Describe the morphology of the red blood cells.
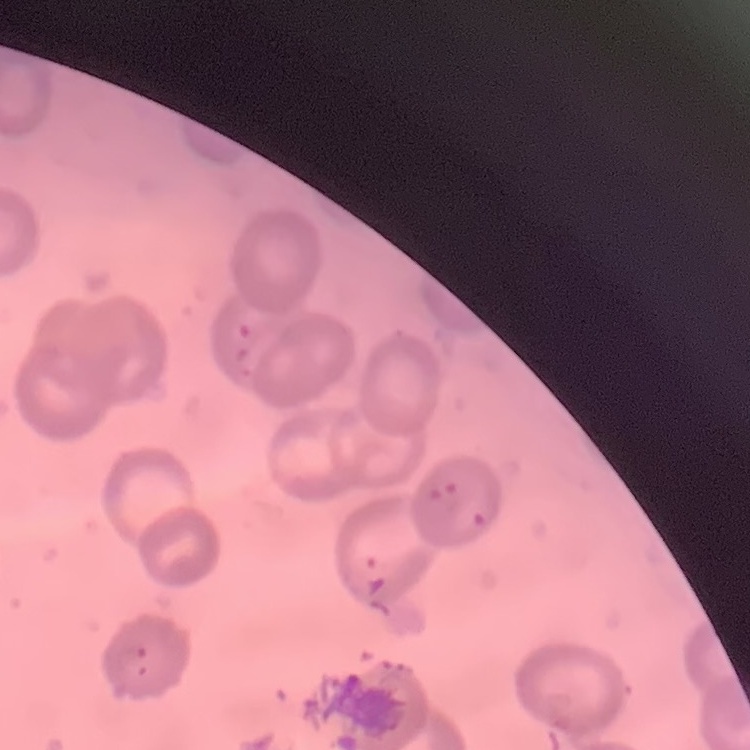
No rouleaux formation.

Summary:
  - Preparation: thin blood smear
  - Image type: one tile cut from a larger photomicrograph
  - Stain: Field's or Giemsa